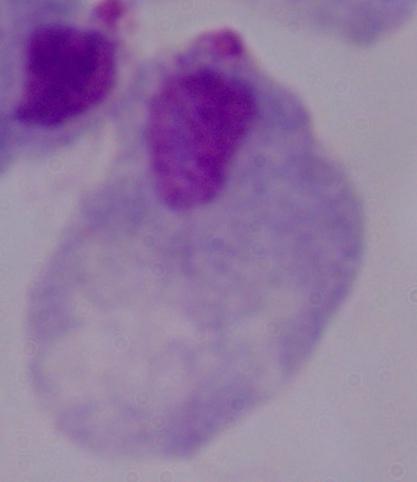
Summary:
  - Magnification: 1000x
  - Modality: micrograph
  - Identification: trichomonad